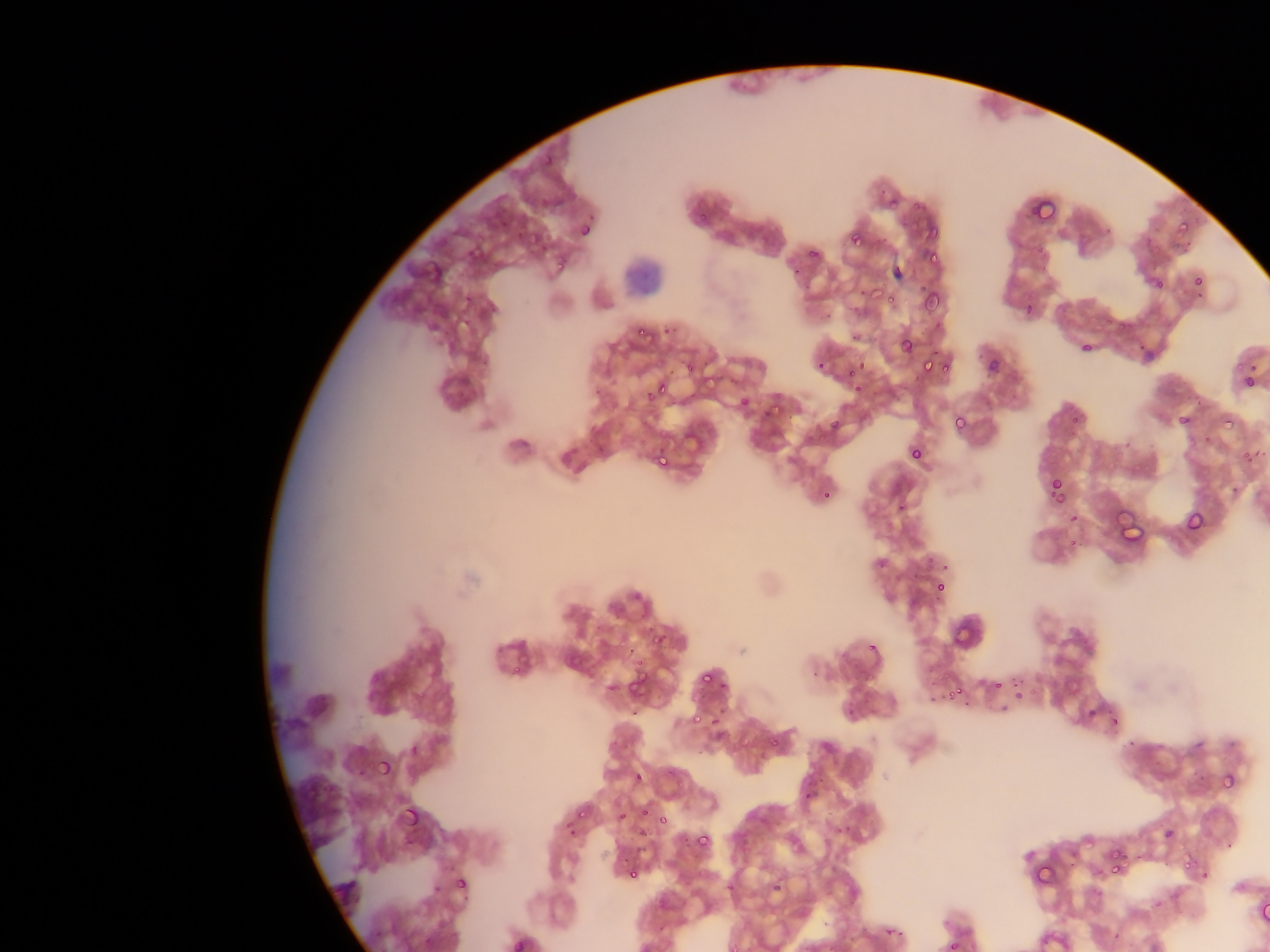

leukocyte locations = approximate bounding boxes as {left, top, right, bottom} in pixels: {622, 256, 658, 297}
image size = 1270×952 pixels
country = Ghana
field of view = single
malaria parasite locations = approximate bounding boxes as {left, top, right, bottom} in pixels: {533, 144, 569, 172}, {886, 197, 898, 208}, {1024, 197, 1054, 218}, {906, 199, 936, 219}, {695, 210, 710, 226}, {1171, 217, 1200, 236}, {578, 221, 594, 239}, {521, 222, 546, 240}, {491, 223, 504, 233}, {916, 224, 946, 250}, {843, 226, 878, 244}, {801, 242, 826, 265}, {467, 245, 484, 266}, {924, 245, 947, 272}, {550, 261, 564, 271}, {1192, 273, 1205, 287}, {1149, 274, 1169, 293}, {868, 279, 887, 302}, {918, 292, 948, 318}, {882, 297, 900, 305}, {1111, 317, 1133, 332}, {630, 322, 653, 339}, {662, 324, 676, 336}, {901, 337, 916, 353}, {1079, 341, 1092, 353}, {844, 357, 870, 382}, {919, 358, 934, 372}, {985, 358, 1000, 374}, {938, 359, 953, 374}, {1242, 373, 1256, 390}, {656, 380, 674, 397}, {592, 385, 602, 396}, {738, 396, 750, 408}, {761, 406, 775, 420}, {1218, 406, 1248, 434}, {1177, 412, 1193, 428}, {952, 413, 968, 433}, {830, 421, 840, 431}, {1240, 436, 1265, 466}, {908, 445, 923, 461}, {657, 456, 669, 469}, {1051, 478, 1064, 494}, {1046, 481, 1064, 499}, {822, 491, 832, 501}, {1185, 511, 1204, 531}, {1068, 513, 1079, 524}, {1118, 515, 1150, 547}, {933, 579, 949, 595}, {951, 610, 981, 647}, {646, 630, 665, 647}, {863, 644, 878, 655}, {630, 660, 649, 670}, {510, 661, 528, 677}, {623, 669, 655, 698}, {700, 672, 715, 689}, {994, 681, 1003, 691}, {944, 687, 967, 699}, {1014, 691, 1024, 701}, {928, 695, 938, 705}, {1084, 706, 1096, 718}, {687, 709, 706, 728}, {711, 712, 724, 726}, {1109, 714, 1120, 727}, {1126, 737, 1137, 748}, {408, 743, 421, 758}, {376, 756, 394, 776}, {1218, 767, 1239, 788}, {632, 771, 644, 784}, {397, 797, 424, 825}, {639, 806, 651, 817}, {578, 808, 590, 818}, {619, 812, 628, 823}, {658, 816, 668, 826}, {565, 821, 579, 836}, {637, 827, 649, 838}, {1163, 827, 1176, 840}, {695, 833, 711, 849}, {1102, 848, 1130, 878}, {1176, 848, 1201, 867}, {624, 861, 643, 880}, {1034, 861, 1070, 891}, {455, 876, 469, 892}, {769, 879, 785, 896}, {1259, 901, 1270, 925}, {510, 935, 528, 952}, {937, 936, 961, 952}
preparation = thin blood film
capture = mobile-phone photograph through a microscope